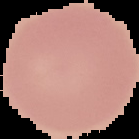

Summary:
  - Preparation: thin blood smear
  - Result: negative for Plasmodium parasites
  - Image type: segmented cell region with the area outside set to black
  - Image size: 139×139 pixels